Assess this cell for malaria.
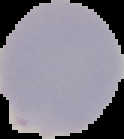
It is uninfected.

Image is 124×139 pixels. Segmented cell region on a black background. From a thin blood film.